Name the cell type shown.
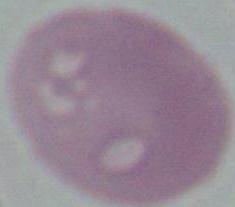

This is an erythrocyte.

Summary:
  - Modality: photomicrograph
  - Magnification: 1000x